Name the cell type shown.
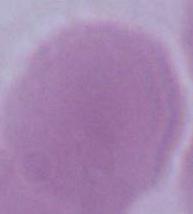

An erythrocyte.

Micrograph. Captured at 1000x magnification.